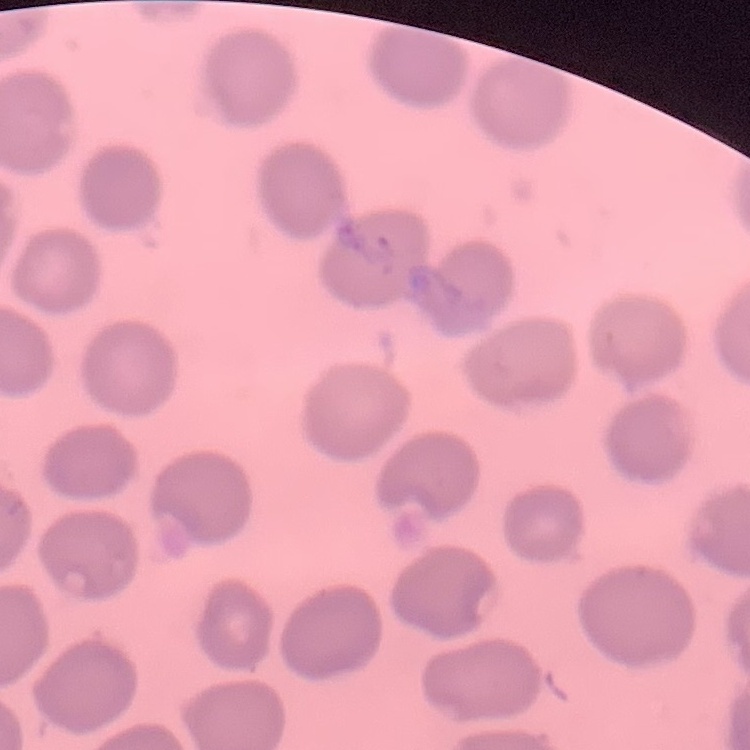

Summary:
  - Red blood cell morphology: no rouleaux formation
  - Preparation: thin blood film
  - Stain: Field's or Giemsa
  - Image type: one tile cut from a larger photomicrograph